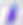
magnification = 400x
modality = photomicrograph
identification = Toxoplasma gondii